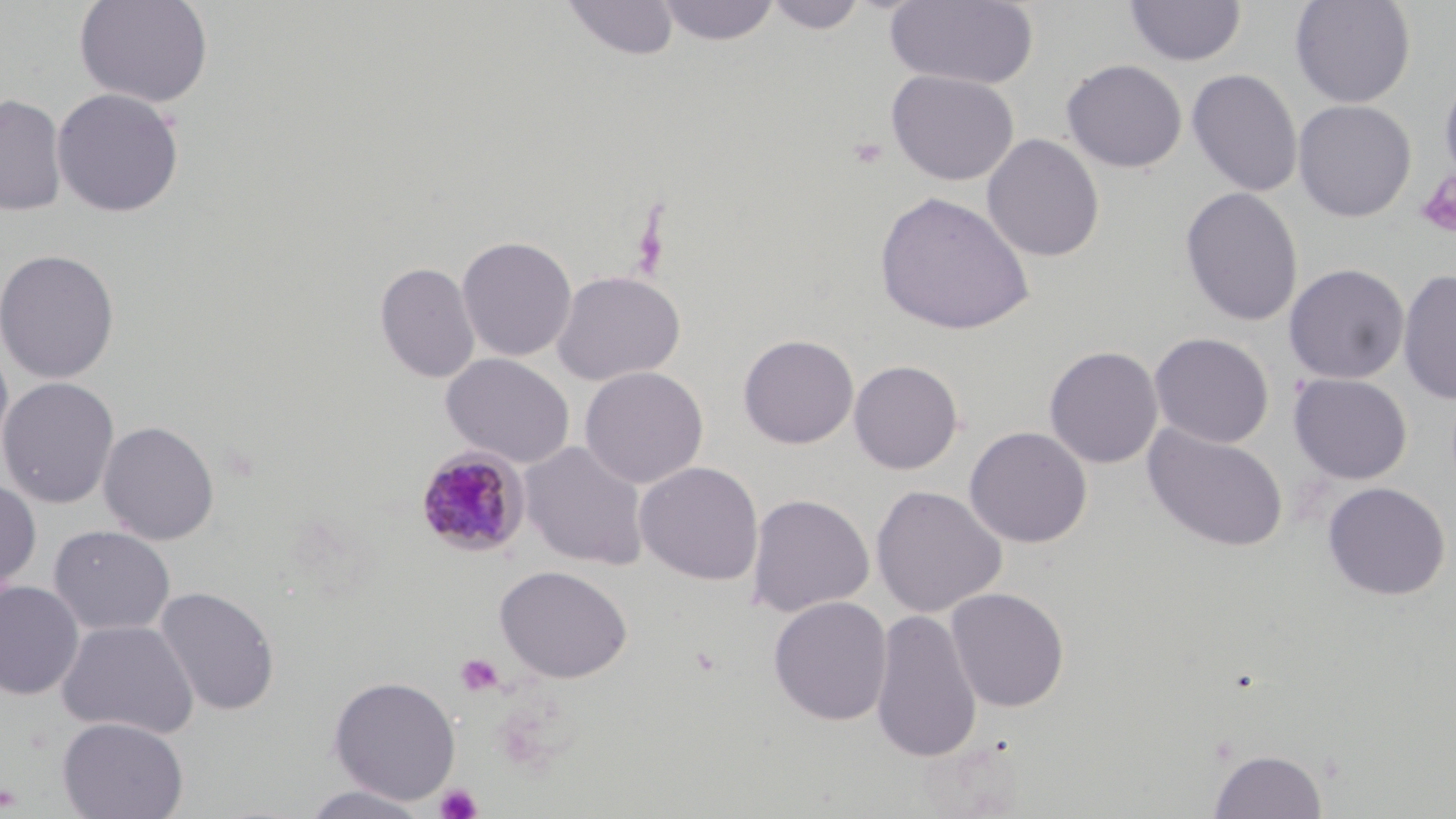
Approximate bounding boxes as named x1/y1/x2/y2 corners in pixels. Plasmodium malariae-infected red blood cell locations: (x1=415, y1=446, x2=530, y2=557). Uninfected red blood cell locations: (x1=73, y1=0, x2=214, y2=108), (x1=562, y1=0, x2=679, y2=61), (x1=763, y1=0, x2=869, y2=34), (x1=885, y1=0, x2=1039, y2=90), (x1=1289, y1=0, x2=1416, y2=108), (x1=655, y1=1, x2=781, y2=46), (x1=1124, y1=1, x2=1246, y2=67), (x1=1062, y1=59, x2=1187, y2=173), (x1=1187, y1=68, x2=1303, y2=197), (x1=1439, y1=68, x2=1456, y2=190), (x1=886, y1=69, x2=1019, y2=186), (x1=52, y1=88, x2=185, y2=218), (x1=0, y1=95, x2=67, y2=216), (x1=1293, y1=99, x2=1416, y2=222), (x1=981, y1=133, x2=1105, y2=262), (x1=1180, y1=187, x2=1304, y2=327), (x1=874, y1=191, x2=1035, y2=336), (x1=456, y1=235, x2=577, y2=362), (x1=0, y1=248, x2=120, y2=384), (x1=375, y1=261, x2=480, y2=383), (x1=1283, y1=263, x2=1409, y2=384), (x1=1398, y1=269, x2=1456, y2=405), (x1=551, y1=270, x2=685, y2=386), (x1=1150, y1=332, x2=1274, y2=448), (x1=738, y1=334, x2=858, y2=449), (x1=0, y1=341, x2=15, y2=470), (x1=1044, y1=346, x2=1163, y2=469), (x1=440, y1=352, x2=576, y2=468), (x1=848, y1=359, x2=964, y2=474), (x1=579, y1=366, x2=709, y2=489), (x1=1289, y1=373, x2=1412, y2=485), (x1=0, y1=377, x2=120, y2=509), (x1=98, y1=420, x2=220, y2=545), (x1=1142, y1=423, x2=1288, y2=552), (x1=964, y1=426, x2=1093, y2=548), (x1=519, y1=441, x2=649, y2=569), (x1=634, y1=461, x2=764, y2=585), (x1=0, y1=478, x2=41, y2=597), (x1=1321, y1=481, x2=1451, y2=600), (x1=871, y1=484, x2=1007, y2=617), (x1=746, y1=493, x2=874, y2=617), (x1=48, y1=525, x2=175, y2=636), (x1=494, y1=565, x2=633, y2=683), (x1=0, y1=581, x2=85, y2=700), (x1=154, y1=586, x2=280, y2=717), (x1=945, y1=587, x2=1070, y2=712), (x1=768, y1=596, x2=893, y2=726), (x1=870, y1=609, x2=982, y2=762), (x1=56, y1=619, x2=198, y2=739), (x1=327, y1=675, x2=461, y2=805), (x1=57, y1=716, x2=188, y2=819), (x1=1208, y1=748, x2=1328, y2=818), (x1=300, y1=785, x2=431, y2=818). Platelet locations: (x1=1416, y1=171, x2=1455, y2=241), (x1=456, y1=653, x2=505, y2=697), (x1=0, y1=781, x2=22, y2=812), (x1=434, y1=783, x2=482, y2=819). Slide-level diagnosis: Plasmodium malariae. May-Grünwald-Giemsa-stained preparation. Optical microscopy. Captured at 1000x magnification. Thin blood smear. Image is 1456×819 pixels. Single field of view.